Assess the morphology of the erythrocytes.
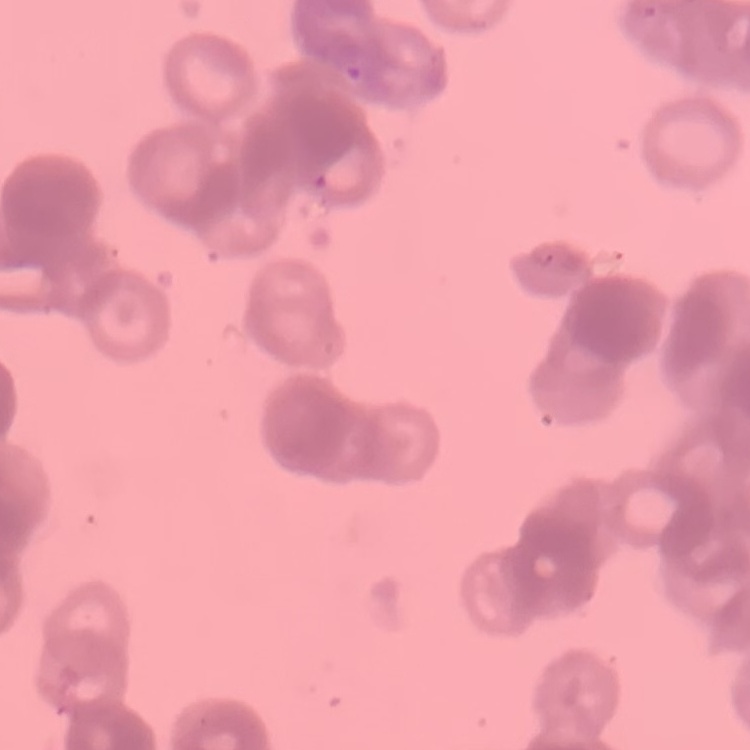
They show rouleaux formation.

stain: Field's or Giemsa
preparation: thin blood smear
image_type: one tile cut from a larger photomicrograph